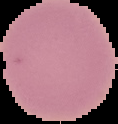

Summary:
  - Result: negative for Plasmodium parasites
  - Image type: segmented cell region on a black background
  - Preparation: thin blood smear
  - Image size: 118×124 pixels